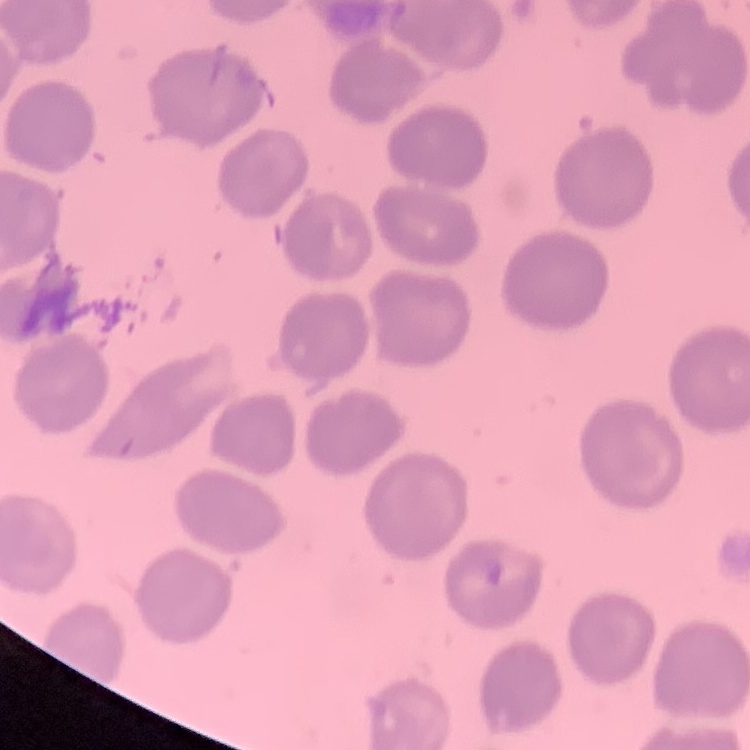
red blood cell morphology = no rouleaux formation
preparation = thin blood film
image type = square crop of a larger photomicrograph
stain = Field's or Giemsa